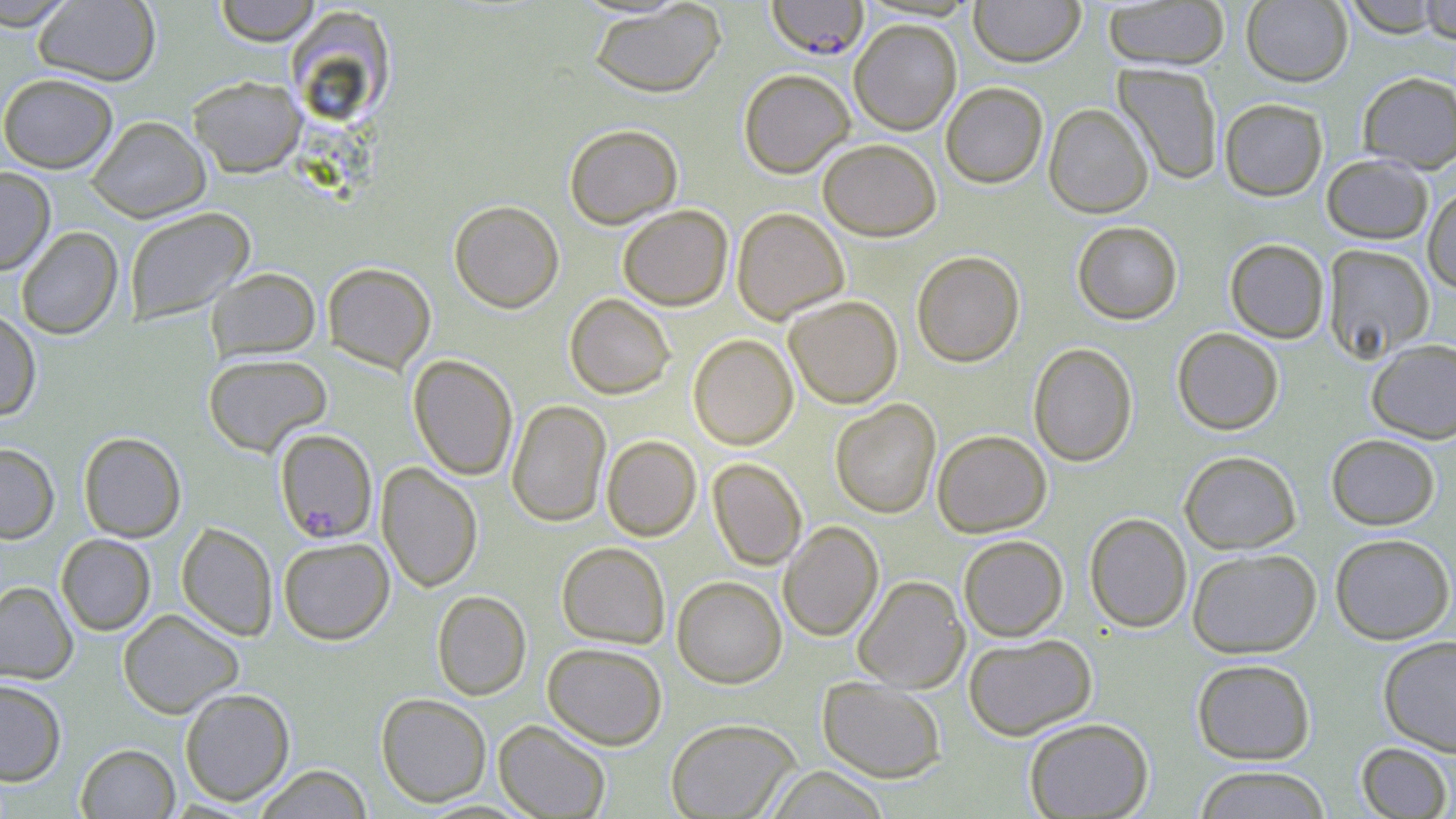
Summary:
  - Coordinate format: approximate bounding boxes as (x1,y1)-(x2,y2) corner pairs in pixels
  - Plasmodium falciparum-infected red blood cell locations: (766,0)-(870,60), (274,428)-(377,543)
  - Uninfected red blood cell locations: (213,0)-(322,46), (969,0)-(1084,67), (1241,0)-(1352,86), (1341,0)-(1450,37), (1418,0)-(1456,42), (0,1)-(78,30), (33,1)-(161,86), (1102,1)-(1231,70), (589,2)-(726,98), (287,7)-(401,124), (849,19)-(962,135), (1113,63)-(1224,185), (738,69)-(855,177), (1357,71)-(1456,173), (0,72)-(118,173), (188,75)-(306,177), (940,81)-(1048,188), (1219,98)-(1328,201), (1043,103)-(1153,218), (86,115)-(211,222), (564,123)-(682,229), (817,138)-(942,240), (1321,154)-(1433,244), (0,166)-(56,275), (1423,183)-(1456,293), (449,200)-(564,313), (618,205)-(733,311), (123,207)-(255,326), (732,207)-(850,324), (1072,221)-(1183,324), (16,227)-(123,340), (1225,238)-(1329,344), (1323,244)-(1434,362), (912,250)-(1025,367), (322,262)-(436,373), (206,267)-(320,361), (564,294)-(675,399), (783,295)-(903,408), (0,308)-(41,421), (1172,328)-(1284,435), (688,334)-(798,450), (1366,338)-(1456,444), (1028,342)-(1137,467), (203,353)-(332,456), (408,354)-(518,480), (830,399)-(941,518), (506,400)-(611,527), (932,430)-(1051,537), (78,431)-(186,542), (1326,433)-(1440,530), (601,435)-(701,541), (0,442)-(60,544), (1179,450)-(1302,554), (707,458)-(807,570), (377,462)-(483,592), (1084,513)-(1192,633), (778,521)-(883,641), (176,523)-(277,641), (1329,533)-(1455,644), (56,534)-(156,635), (958,535)-(1068,641), (278,537)-(395,645), (556,542)-(670,648), (1187,548)-(1321,658), (853,575)-(970,693), (672,576)-(787,688), (0,581)-(78,684), (432,591)-(531,700), (117,608)-(244,719), (963,634)-(1097,740), (1378,635)-(1456,755), (543,642)-(667,749), (1192,658)-(1316,765), (817,677)-(946,782), (0,679)-(67,786), (179,687)-(295,806), (375,692)-(492,807), (665,717)-(802,819), (1024,717)-(1153,818), (494,720)-(611,818), (1356,742)-(1453,818), (76,743)-(180,818), (253,764)-(374,818), (1192,765)-(1332,818), (764,766)-(890,819)
  - Slide-level diagnosis: Plasmodium falciparum
  - Modality: light microscopy
  - Image size: 1456×819 pixels
  - Preparation: thin blood smear
  - Magnification: 1000x
  - Stain: May-Grünwald-Giemsa
  - Field of view: one of a larger specimen